Name the blood parasite species.
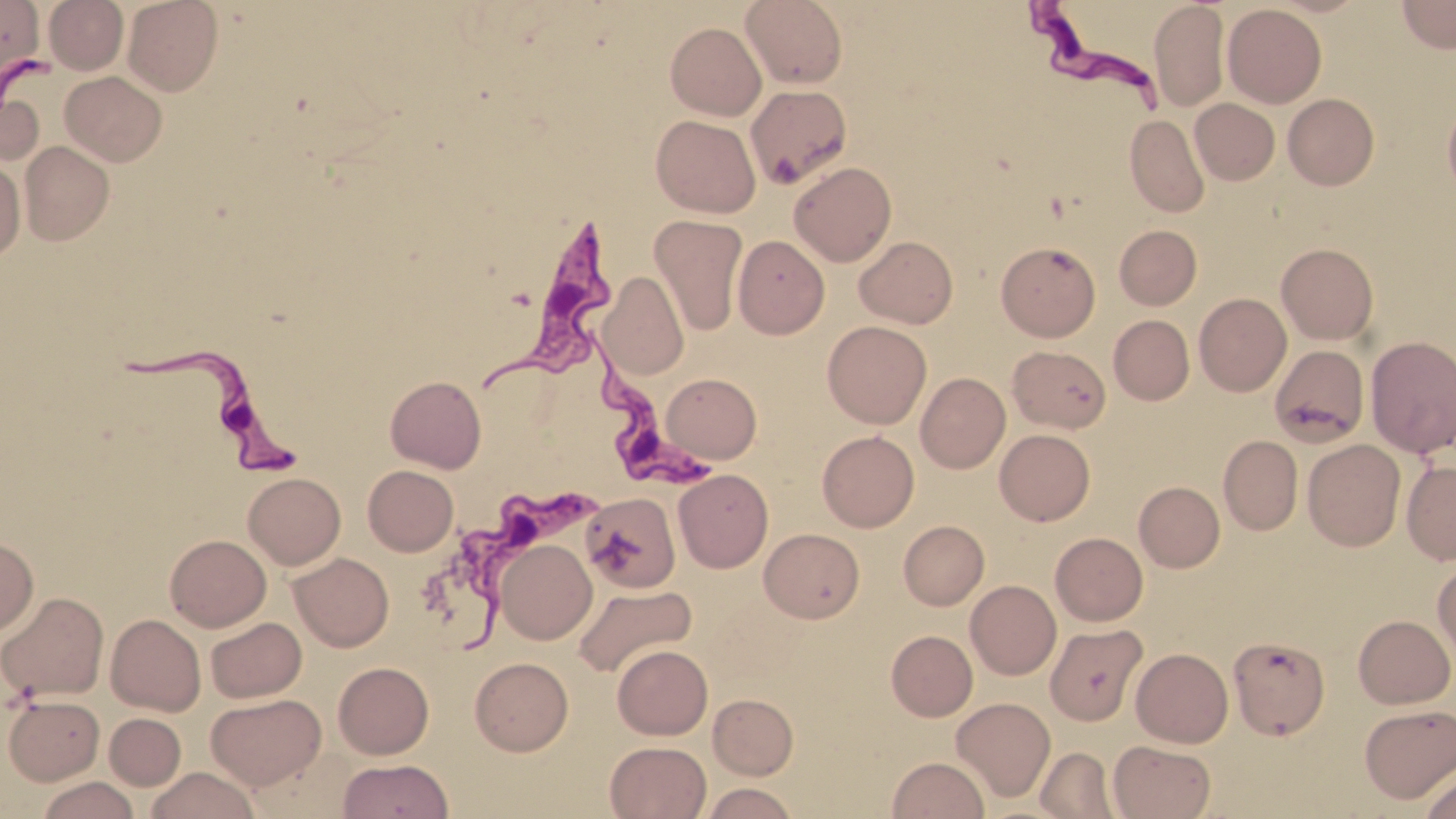
Trypanosoma brucei.

image size = 1456×819 pixels
Trypanosoma brucei locations = approximate bounding boxes as named x1/y1/x2/y2 corners in pixels: (x1=1023, y1=0, x2=1174, y2=116), (x1=491, y1=216, x2=623, y2=395), (x1=126, y1=329, x2=303, y2=466), (x1=583, y1=333, x2=719, y2=498), (x1=452, y1=487, x2=611, y2=659)
field of view = one of a larger specimen
preparation = thin blood film
modality = optical microscopy
stain = May-Grünwald-Giemsa
uninfected red blood cell locations = approximate bounding boxes as named x1/y1/x2/y2 corners in pixels: (x1=0, y1=0, x2=50, y2=66), (x1=44, y1=0, x2=128, y2=74), (x1=123, y1=0, x2=223, y2=96), (x1=740, y1=0, x2=848, y2=89), (x1=1397, y1=0, x2=1456, y2=54), (x1=1149, y1=1, x2=1229, y2=112), (x1=1222, y1=4, x2=1326, y2=107), (x1=665, y1=22, x2=766, y2=120), (x1=59, y1=71, x2=167, y2=166), (x1=746, y1=85, x2=853, y2=189), (x1=0, y1=86, x2=44, y2=168), (x1=1283, y1=93, x2=1379, y2=190), (x1=1443, y1=95, x2=1456, y2=203), (x1=1190, y1=98, x2=1280, y2=185), (x1=1125, y1=114, x2=1210, y2=218), (x1=651, y1=115, x2=760, y2=217), (x1=19, y1=141, x2=114, y2=245), (x1=0, y1=158, x2=26, y2=261), (x1=789, y1=162, x2=897, y2=266), (x1=649, y1=215, x2=749, y2=336), (x1=1114, y1=225, x2=1202, y2=310), (x1=732, y1=235, x2=829, y2=338), (x1=855, y1=236, x2=958, y2=328), (x1=996, y1=242, x2=1101, y2=341), (x1=1276, y1=243, x2=1379, y2=344), (x1=599, y1=271, x2=690, y2=381), (x1=1194, y1=293, x2=1291, y2=396), (x1=1109, y1=315, x2=1194, y2=405), (x1=822, y1=321, x2=932, y2=428), (x1=1365, y1=335, x2=1456, y2=457), (x1=1008, y1=345, x2=1110, y2=433), (x1=1279, y1=352, x2=1371, y2=451), (x1=915, y1=372, x2=1010, y2=473), (x1=661, y1=373, x2=761, y2=463), (x1=385, y1=375, x2=486, y2=472), (x1=995, y1=429, x2=1095, y2=526), (x1=817, y1=430, x2=919, y2=532), (x1=1219, y1=435, x2=1303, y2=536), (x1=1302, y1=439, x2=1406, y2=551), (x1=1402, y1=460, x2=1456, y2=566), (x1=363, y1=465, x2=458, y2=556), (x1=673, y1=469, x2=773, y2=573), (x1=243, y1=473, x2=345, y2=569), (x1=1134, y1=482, x2=1224, y2=572), (x1=579, y1=492, x2=681, y2=593), (x1=898, y1=520, x2=989, y2=610), (x1=759, y1=528, x2=864, y2=623), (x1=1050, y1=532, x2=1147, y2=625), (x1=165, y1=535, x2=271, y2=631), (x1=0, y1=537, x2=38, y2=637), (x1=495, y1=540, x2=597, y2=644), (x1=289, y1=553, x2=394, y2=652), (x1=1433, y1=559, x2=1456, y2=664), (x1=965, y1=580, x2=1061, y2=680), (x1=572, y1=583, x2=696, y2=679), (x1=1, y1=591, x2=109, y2=702), (x1=105, y1=614, x2=206, y2=716), (x1=1353, y1=614, x2=1455, y2=708), (x1=205, y1=617, x2=306, y2=703), (x1=1045, y1=624, x2=1148, y2=725), (x1=886, y1=630, x2=978, y2=721), (x1=1228, y1=636, x2=1330, y2=740), (x1=612, y1=644, x2=713, y2=739), (x1=1131, y1=648, x2=1233, y2=747), (x1=470, y1=657, x2=573, y2=756), (x1=333, y1=662, x2=434, y2=759), (x1=206, y1=693, x2=326, y2=789), (x1=708, y1=694, x2=798, y2=780), (x1=3, y1=695, x2=105, y2=785), (x1=951, y1=697, x2=1055, y2=801), (x1=1359, y1=704, x2=1456, y2=803), (x1=104, y1=713, x2=186, y2=790), (x1=605, y1=741, x2=711, y2=819), (x1=1109, y1=741, x2=1217, y2=819), (x1=1034, y1=746, x2=1118, y2=818), (x1=887, y1=756, x2=989, y2=818), (x1=339, y1=759, x2=452, y2=818), (x1=1420, y1=765, x2=1456, y2=818), (x1=145, y1=767, x2=261, y2=819), (x1=38, y1=776, x2=138, y2=819), (x1=700, y1=783, x2=799, y2=819)
magnification = 1000x